State which cell type is depicted.
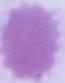
This is an erythrocyte.

Summary:
  - Magnification: 1000x
  - Modality: micrograph